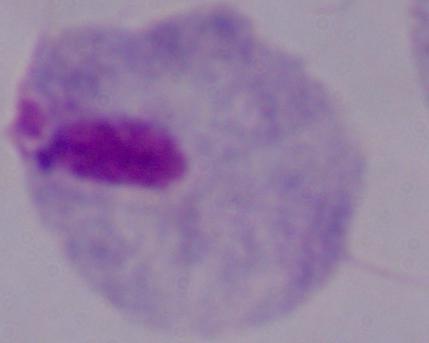
Summary:
  - Magnification: 1000x
  - Modality: micrograph
  - Identification: trichomonad